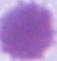
Summary:
  - Identification: red blood cell
  - Modality: micrograph
  - Magnification: 1000x